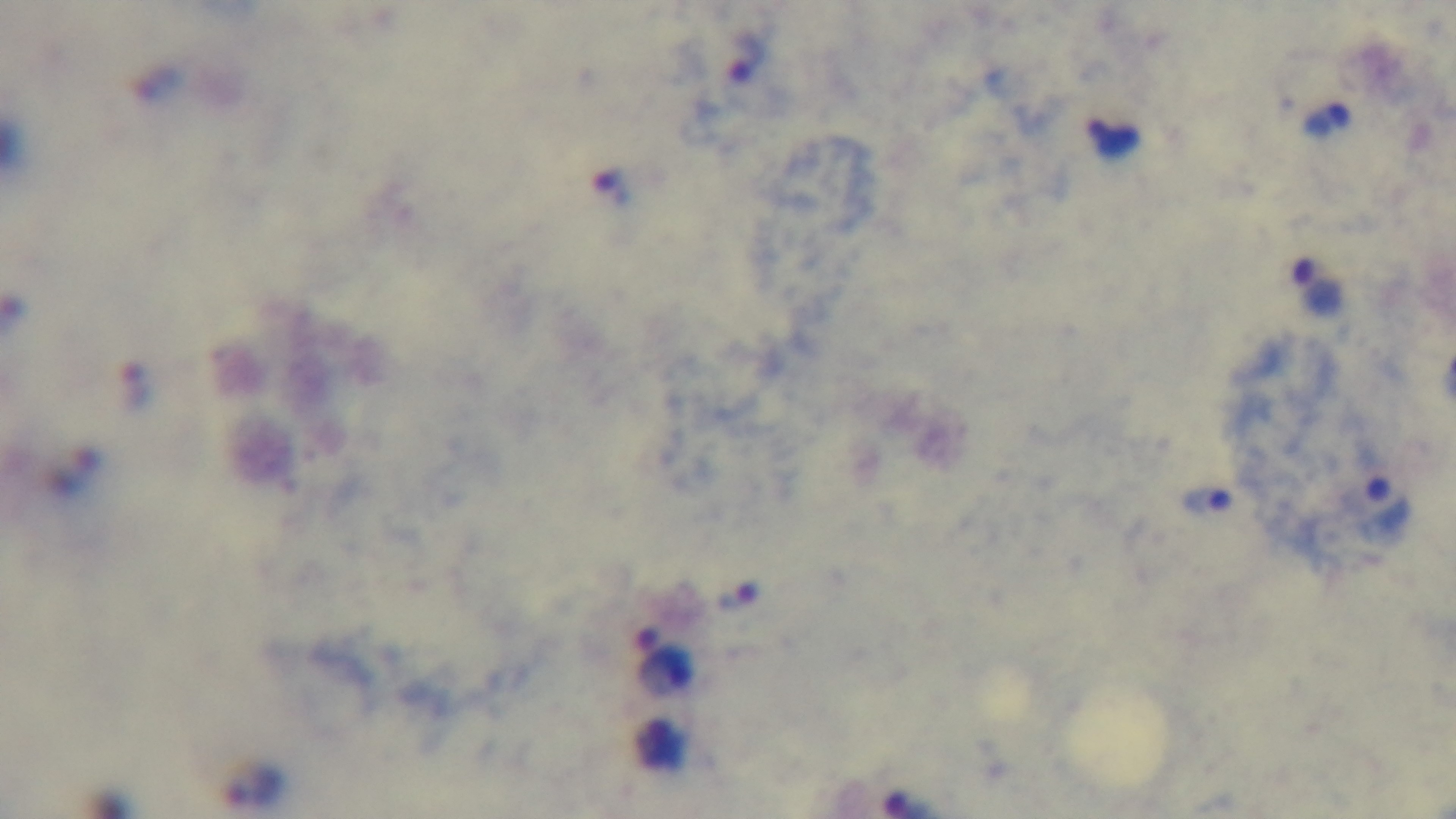

Summary:
  - Modality: light microscopy
  - Malaria status: positive
  - Stain: Giemsa
  - Preparation: thick blood film
  - Field of view: single
  - Objective: 100x oil immersion
  - Capture: mounted 4K digital camera